Outline every malaria parasite, every leukocyte, and every artifact (stain precipitate or debris).
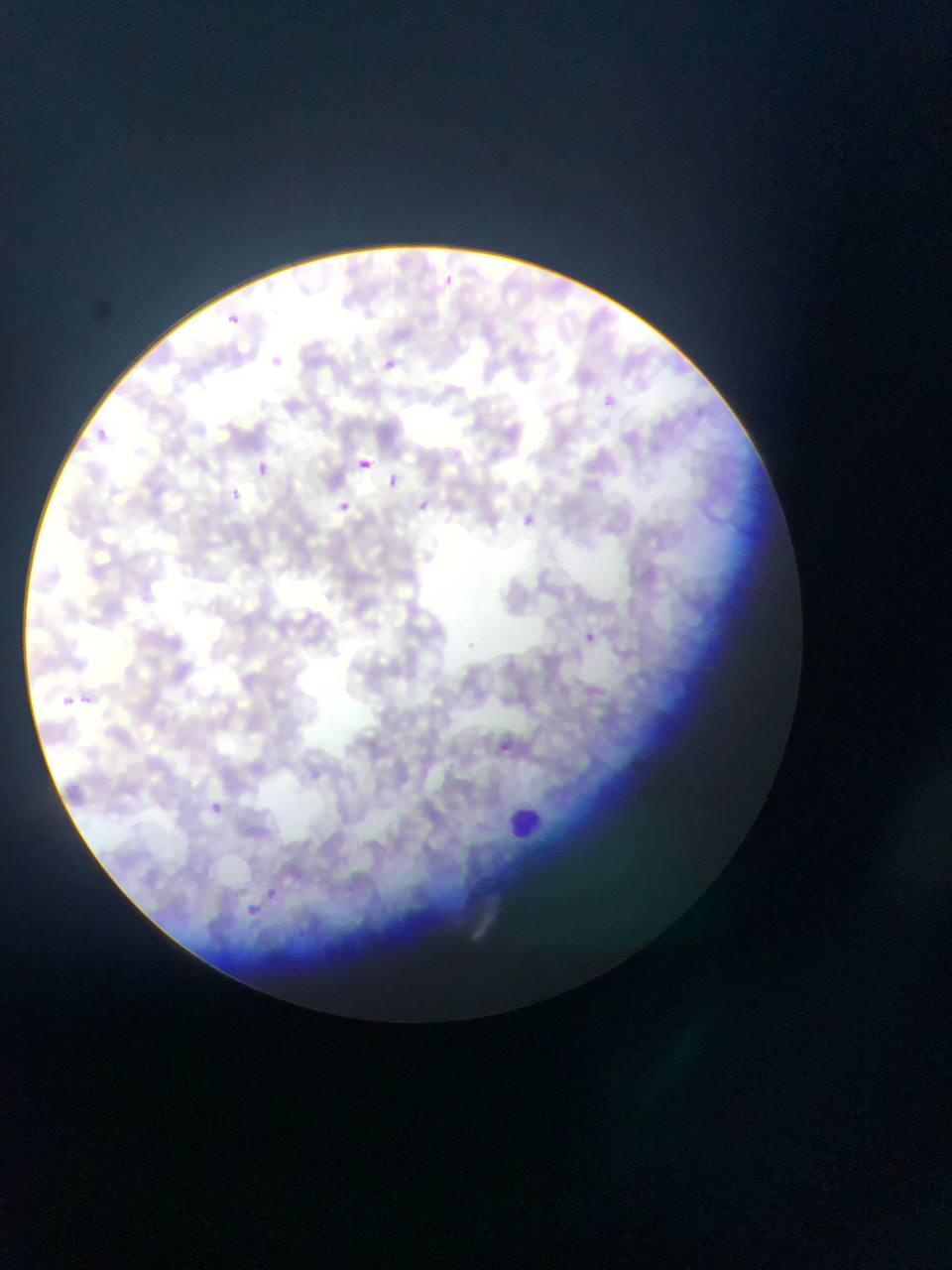

Approximate bounding boxes as (left, top, right, bottom) in pixels.
Malaria parasites: (437, 271, 469, 301), (219, 302, 255, 334), (262, 348, 292, 379), (379, 354, 399, 374), (603, 387, 625, 424), (88, 420, 110, 440), (353, 452, 370, 475), (256, 460, 270, 476), (381, 466, 410, 495), (230, 488, 240, 500), (329, 494, 355, 520), (408, 494, 435, 518), (519, 509, 538, 526), (580, 620, 603, 646), (80, 693, 95, 705), (62, 694, 76, 706), (489, 728, 520, 762), (206, 794, 225, 813), (264, 878, 283, 903), (237, 894, 262, 917).
Leukocytes: (499, 804, 562, 844).

Single field of view. Sample from Ghana. Thin blood film. Photographed through a microscope with a mobile-phone camera. Image is 952×1270 pixels.